State the preparation type.
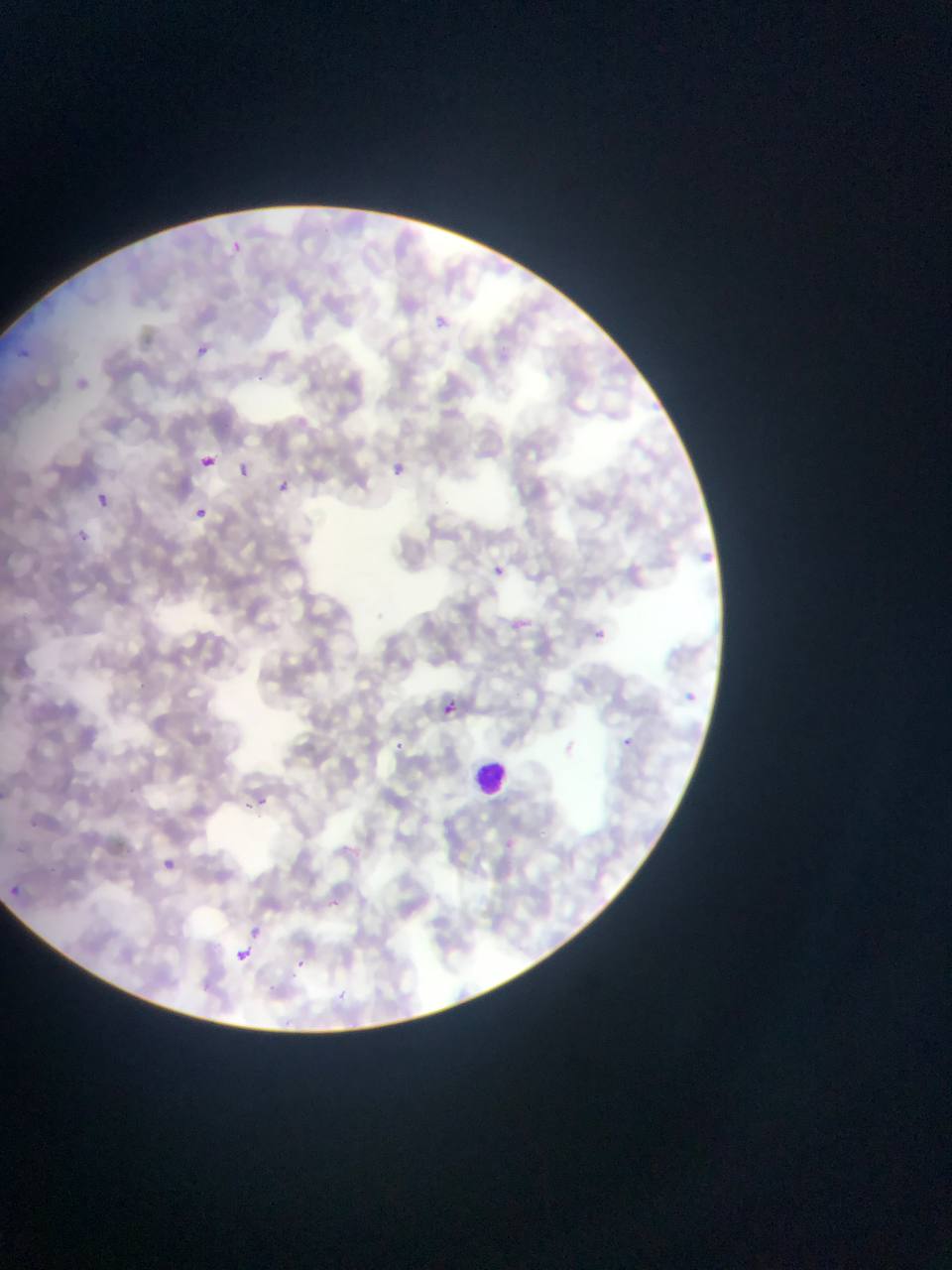

This is a thin smear.

Approximate bounding boxes as {left, top, right, bottom} in pixels.
Summary:
  - Leukocyte locations: {475, 750, 507, 798}
  - Plasmodium parasite locations: {227, 241, 254, 260}, {199, 344, 224, 370}, {18, 349, 30, 359}, {196, 455, 214, 472}, {390, 457, 407, 481}, {235, 461, 254, 488}, {280, 475, 298, 499}, {97, 492, 110, 506}, {196, 506, 207, 517}, {78, 530, 88, 541}, {491, 561, 503, 579}, {576, 620, 600, 645}, {686, 685, 703, 716}, {442, 703, 456, 714}, {618, 729, 635, 747}, {392, 735, 399, 750}, {254, 790, 265, 808}, {164, 859, 176, 868}, {11, 875, 38, 893}, {245, 917, 265, 944}, {228, 949, 258, 975}
  - Capture: mobile-phone photograph through a microscope
  - Image size: 952×1270 pixels
  - Country: Ghana
  - Field of view: single